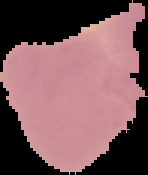
Result: negative for malaria parasites. Image is 148×175 pixels. From a thin blood smear. Cell region segmented out of the field of view; the surrounding area is masked to black.